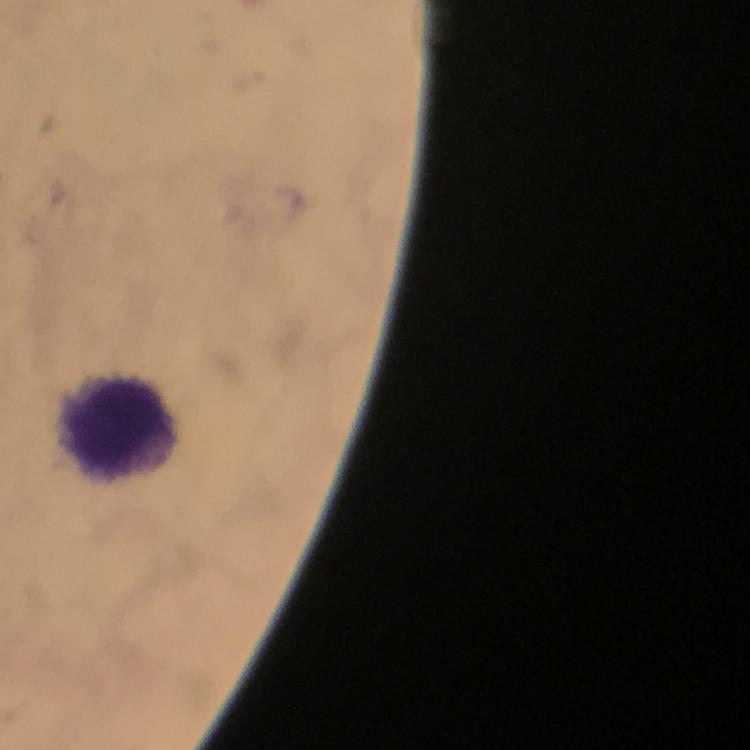
Approximate object centers, in pixels from the top-left corner.
Summary:
  - Leukocyte locations: (x=119, y=430)
  - Plasmodium parasites: none detected
  - Stain: Giemsa
  - Capture: smartphone camera through the microscope
  - Context: from a malaria diagnostic workup
  - Preparation: thick smear
  - Magnification: 100x
  - Immersion oil: used
  - Cropped from: a single field of view
  - Image size: 750×750 pixels